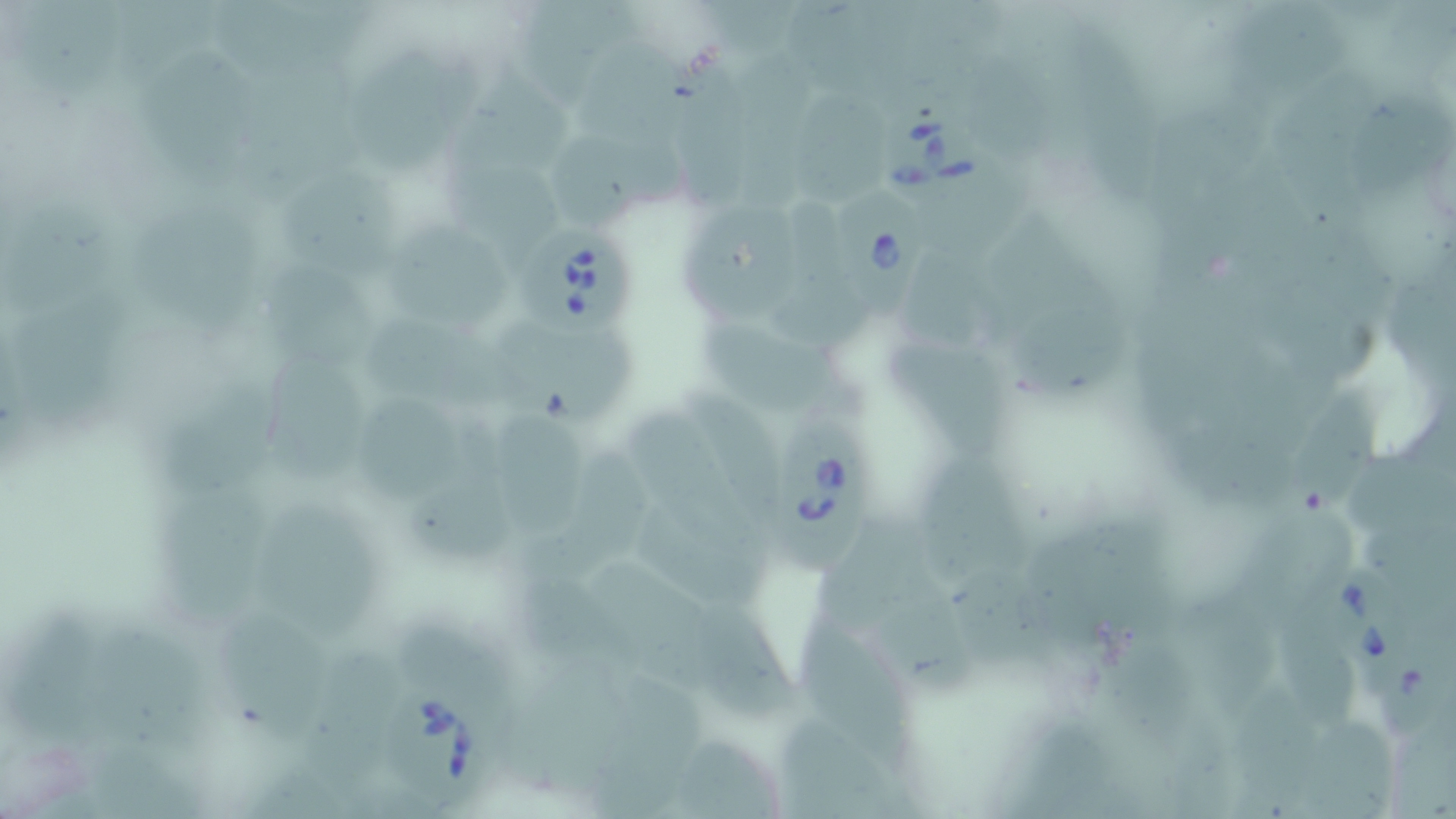

Summary:
  - Coordinate format: approximate bounding boxes as (x1,y1)-(x2,y2) corner pairs in pixels
  - Babesia divergens-infected red blood cell locations: (885,110)-(996,212), (837,181)-(928,317), (519,228)-(631,338), (768,408)-(867,578), (1325,564)-(1398,676), (386,690)-(505,804)
  - Uninfected red blood cell locations: (712,0)-(804,57), (119,3)-(214,94), (796,5)-(918,90), (19,6)-(133,97), (224,6)-(387,73), (524,6)-(649,96), (1253,9)-(1345,100), (971,35)-(1059,164), (1082,37)-(1164,196), (589,51)-(713,148), (732,51)-(819,216), (154,57)-(273,183), (365,59)-(476,176), (677,65)-(767,219), (248,66)-(377,214), (457,66)-(582,179), (1288,76)-(1373,212), (1349,86)-(1444,195), (812,96)-(901,216), (1177,96)-(1268,180), (551,133)-(693,233), (1229,143)-(1318,286), (1153,167)-(1235,283), (452,169)-(567,261), (294,177)-(416,282), (933,184)-(1024,263), (767,194)-(863,341), (0,195)-(126,317), (131,202)-(268,340), (693,214)-(810,313), (1008,223)-(1109,318), (394,227)-(507,316), (1312,235)-(1401,329), (1390,247)-(1456,395), (892,251)-(1011,357), (271,258)-(379,373), (1153,285)-(1223,427), (1299,293)-(1374,391), (4,294)-(141,435), (1030,303)-(1131,408), (698,306)-(838,407), (385,314)-(524,411), (504,330)-(631,431), (896,330)-(1012,458), (265,361)-(373,497), (158,377)-(279,494), (1292,379)-(1371,511), (690,387)-(783,507), (365,395)-(458,503), (405,395)-(519,565), (505,400)-(589,530), (1347,411)-(1453,542), (627,416)-(755,553), (524,435)-(652,589), (928,456)-(1035,591), (158,491)-(259,632), (267,503)-(381,660), (1253,503)-(1361,620), (649,514)-(763,608), (1030,517)-(1172,637), (820,525)-(933,629), (589,538)-(721,708), (967,574)-(1058,698), (881,578)-(968,706), (1192,578)-(1288,727), (519,586)-(642,688), (16,601)-(114,726), (804,602)-(906,750), (708,605)-(798,727), (209,608)-(314,727), (406,615)-(505,706), (96,616)-(205,725), (1294,625)-(1367,731), (1382,625)-(1456,734), (1115,645)-(1197,774), (311,654)-(397,763), (617,672)-(713,773), (501,683)-(607,798), (1237,691)-(1322,814), (782,713)-(877,819), (582,715)-(684,819), (1392,721)-(1456,819), (1306,722)-(1397,818), (1027,730)-(1111,819), (682,735)-(774,819), (92,741)-(221,819)
  - Slide-level diagnosis: Babesia divergens
  - Stain: May-Grünwald-Giemsa
  - Magnification: 1000x
  - Modality: optical microscopy
  - Field of view: single
  - Preparation: thin blood smear
  - Image size: 1456×819 pixels